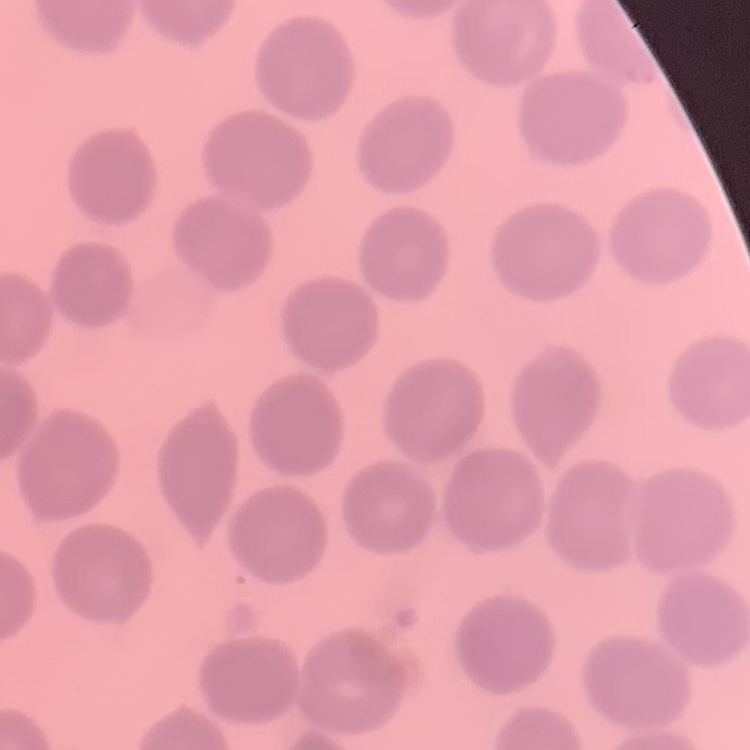

Summary:
  - Red blood cell morphology: no rouleaux formation
  - Preparation: thin blood film
  - Stain: Field's or Giemsa
  - Image type: square crop of a larger photomicrograph